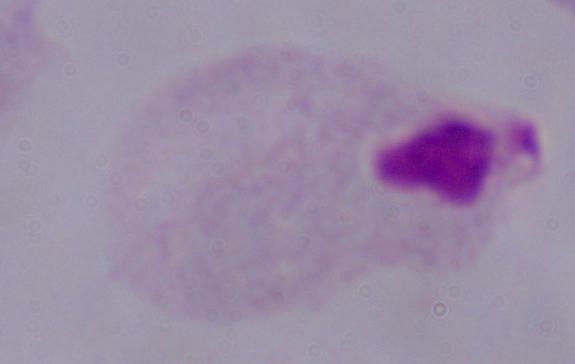

identification = trichomonad
magnification = 1000x
modality = photomicrograph